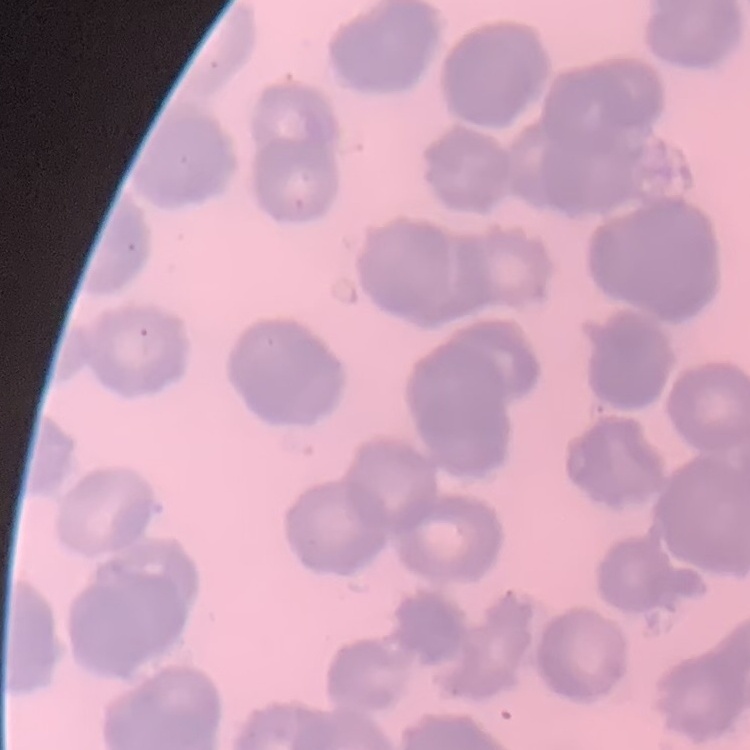

Summary:
  - Erythrocyte morphology: rouleaux formation
  - Stain: Field's or Giemsa
  - Preparation: thin blood smear
  - Image type: square crop of a larger photomicrograph